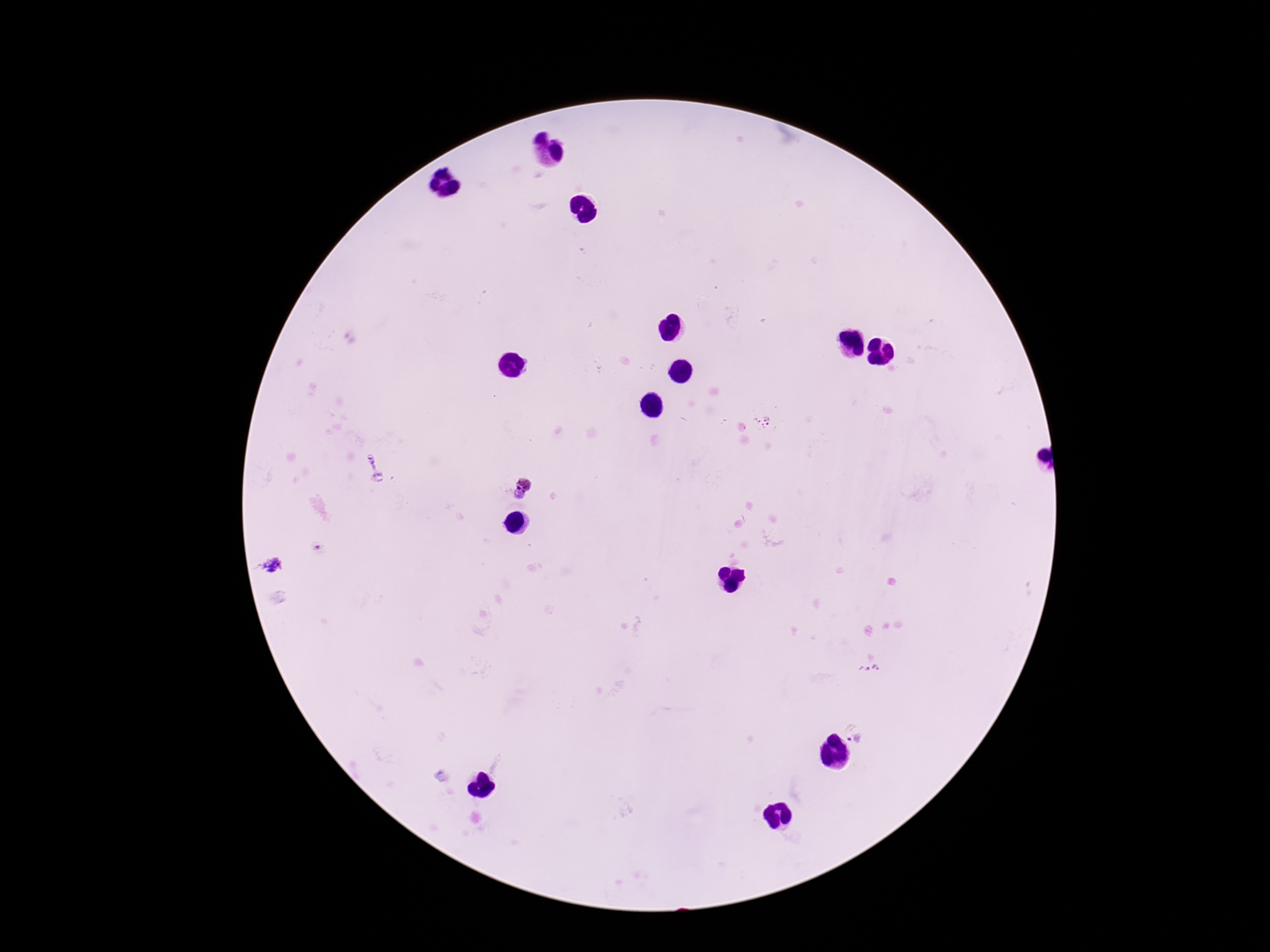

Approximate centers as [x, y] in pixels.
Summary:
  - Plasmodium parasite locations: [764, 422], [373, 465], [520, 488], [316, 547], [273, 565], [869, 670], [856, 739], [442, 774]
  - Image size: 1270×952 pixels
  - Preparation: thick blood film
  - Stain: Giemsa
  - Capture: smartphone camera through the microscope eyepiece
  - Patient malaria status: positive
  - Magnification: 100x
  - Field of view: one from this slide